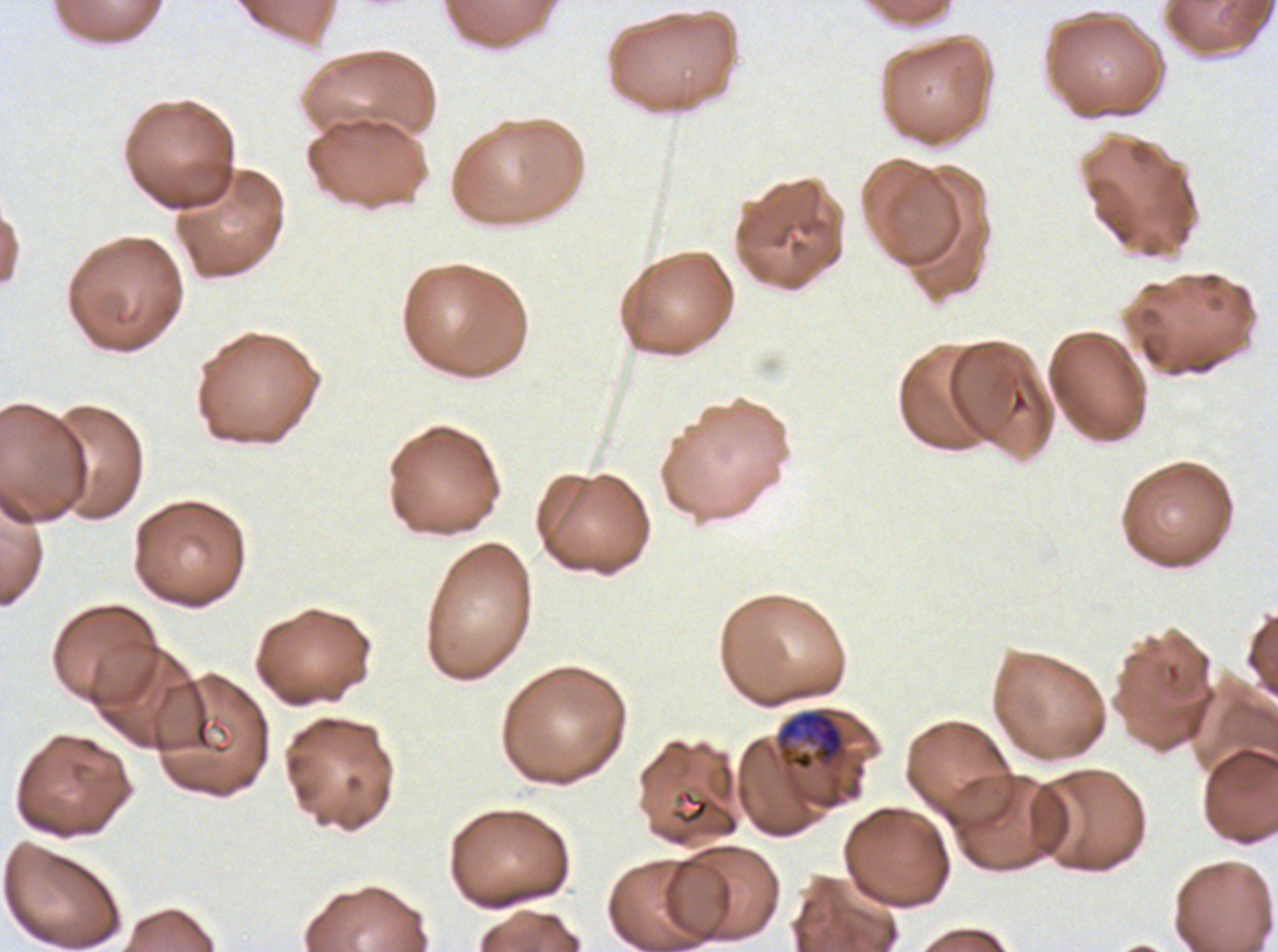

notation = approximate bounding boxes as [x1, y1, x2, y2] in pixels
late trophozoite locations = [777, 710, 845, 771]
debris locations = [672, 788, 711, 826]
field of view = one sub-image of a larger composite
stain = Giemsa
specimen = P. falciparum from a patient in The Gambia, cultured ex vivo for 24 to 48 hours
image size = 1278×952 pixels
preparation = thin blood smear